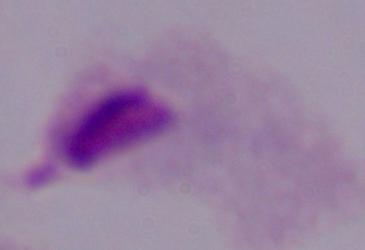

A trichomonad is shown. Micrograph. Captured at 1000x magnification.